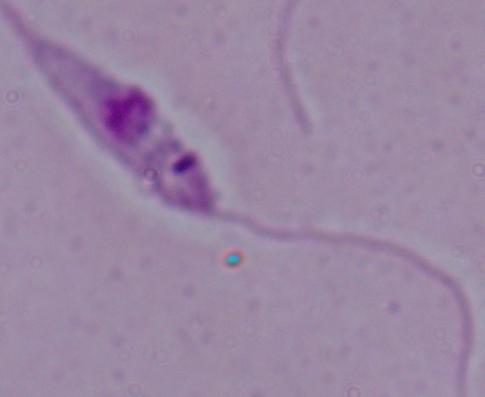

Summary:
  - Identification: Leishmania
  - Modality: photomicrograph
  - Magnification: 1000x